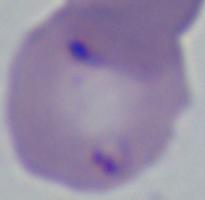

identification = Babesia
modality = photomicrograph
magnification = 1000x